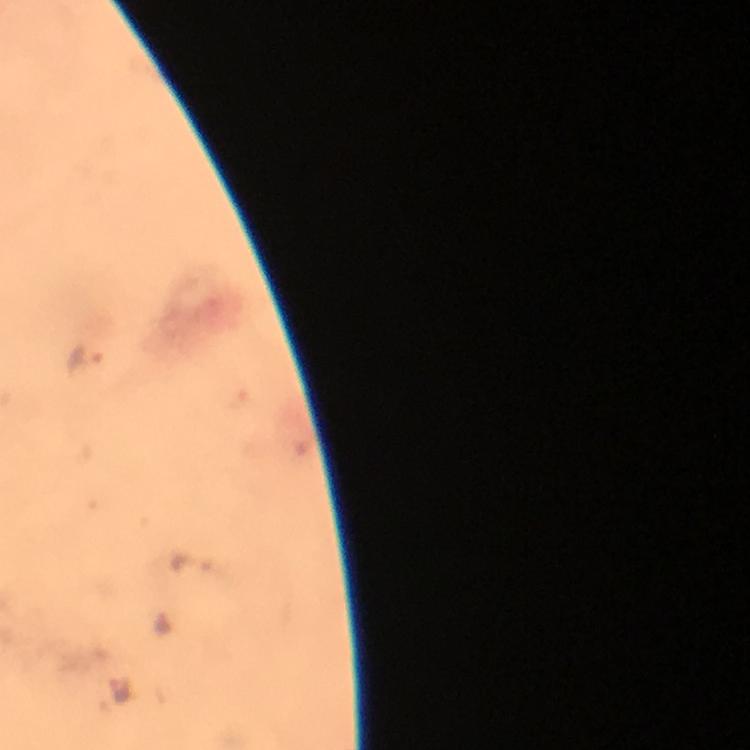
magnification = 100x
stain = Giemsa
malaria parasite locations = approximate centers as [x, y] in pixels: [88, 359], [192, 564], [164, 622], [116, 687]
immersion oil = used
context = from a diagnostic examination for malaria
image size = 750×750 pixels
capture = smartphone mounted on the microscope
preparation = thick blood film
cropped from = one field of view